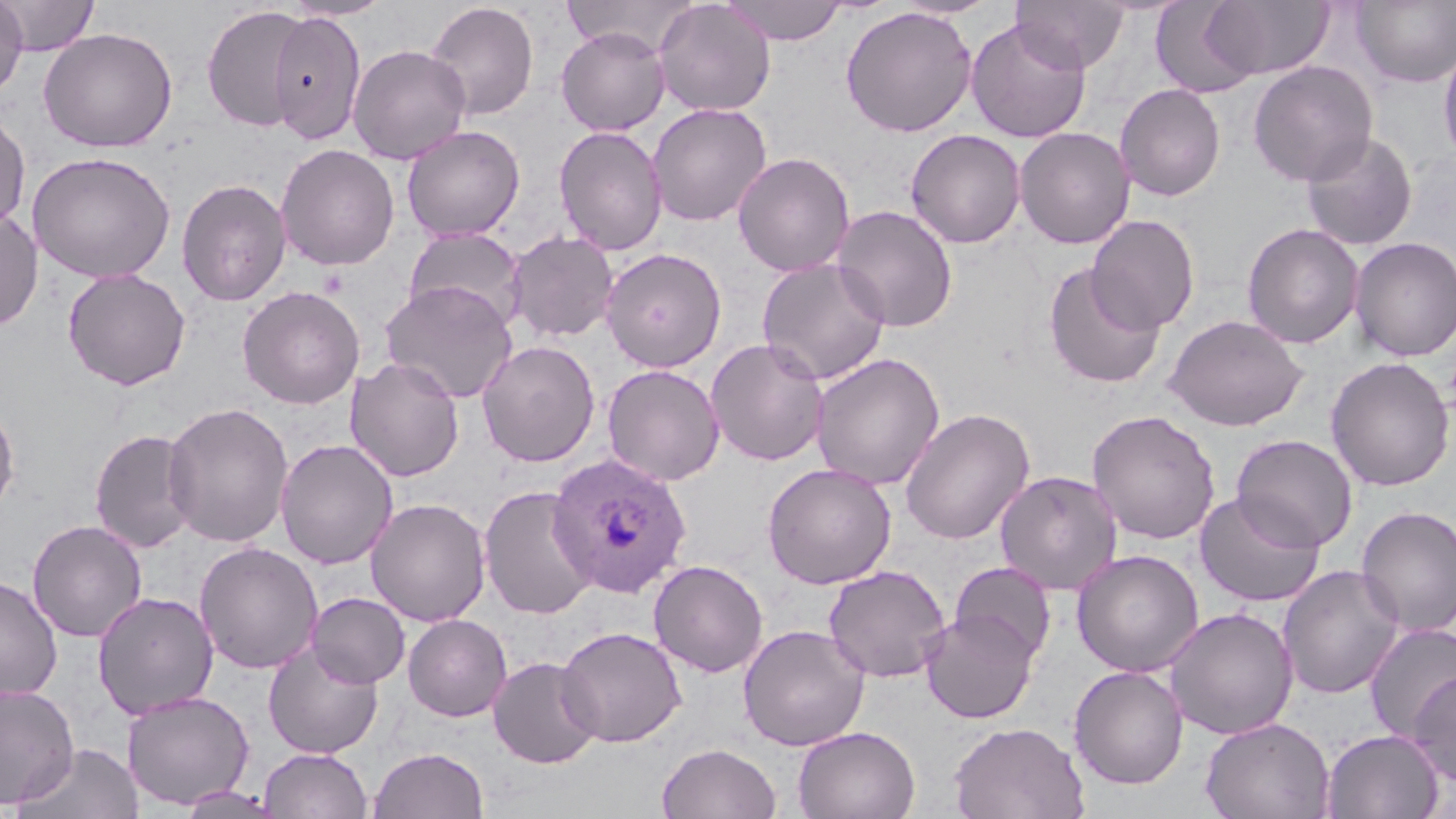

Summary:
  - Coordinate format: approximate bounding boxes as (x1,y1)-(x2,y2) corner pairs in pixels
  - Plasmodium ovale-infected red blood cell locations: (547,453)-(692,598)
  - Uninfected red blood cell locations: (0,0)-(28,100), (2,0)-(100,56), (282,0)-(394,21), (561,0)-(697,56), (721,0)-(847,45), (888,0)-(1001,19), (1012,0)-(1130,73), (1201,0)-(1334,81), (1352,0)-(1456,88), (425,1)-(540,120), (654,1)-(776,116), (1149,1)-(1261,97), (202,5)-(308,132), (840,6)-(977,137), (268,10)-(367,145), (966,18)-(1091,143), (556,26)-(670,136), (38,27)-(178,152), (1438,40)-(1456,167), (348,44)-(471,165), (1247,60)-(1379,186), (1114,83)-(1226,201), (647,102)-(772,226), (0,109)-(31,233), (401,124)-(525,241), (553,125)-(667,256), (1014,126)-(1135,249), (905,129)-(1026,248), (1300,131)-(1417,251), (276,143)-(400,271), (27,151)-(176,283), (733,152)-(855,276), (176,178)-(291,306), (830,205)-(958,332), (0,209)-(44,331), (1086,215)-(1200,334), (1242,223)-(1365,349), (403,226)-(528,332), (506,231)-(619,342), (1350,236)-(1456,362), (601,248)-(726,372), (757,258)-(891,385), (1042,263)-(1166,389), (62,268)-(191,391), (380,280)-(518,403), (237,286)-(365,409), (1164,313)-(1308,431), (705,338)-(831,466), (476,340)-(600,467), (810,352)-(946,490), (345,356)-(465,482), (1326,356)-(1454,492), (602,364)-(725,486), (0,400)-(20,518), (162,402)-(295,547), (900,407)-(1035,545), (1087,409)-(1221,545), (89,429)-(200,553), (1231,434)-(1357,552), (275,438)-(398,569), (762,462)-(897,589), (994,470)-(1123,595), (478,485)-(599,619), (1194,491)-(1326,607), (366,498)-(491,627), (1355,505)-(1456,637), (27,519)-(147,642), (194,541)-(323,674), (1071,549)-(1205,677), (648,559)-(768,677), (950,561)-(1056,665), (1278,563)-(1405,700), (823,565)-(951,683), (0,575)-(63,702), (92,591)-(218,719), (307,592)-(410,688), (1164,607)-(1298,740), (920,609)-(1039,724), (402,614)-(512,722), (1363,622)-(1456,742), (737,624)-(870,751), (555,625)-(687,747), (263,640)-(384,759), (487,656)-(603,769), (1069,665)-(1189,790), (1408,669)-(1456,789), (0,682)-(79,807), (121,690)-(255,810), (1201,716)-(1335,819), (948,721)-(1089,819), (793,725)-(920,819), (1320,729)-(1446,819), (14,743)-(143,819), (657,743)-(782,819), (368,746)-(489,819), (258,748)-(373,819), (178,788)-(283,819)
  - Slide-level diagnosis: Plasmodium ovale
  - Magnification: 1000x
  - Image size: 1456×819 pixels
  - Modality: optical microscopy
  - Preparation: thin blood smear
  - Field of view: single
  - Stain: May-Grünwald-Giemsa